Name the parasite shown.
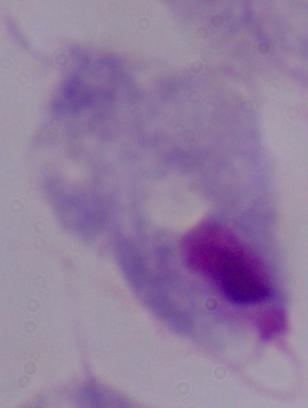

A trichomonad.

Photomicrograph. 1000x magnification.